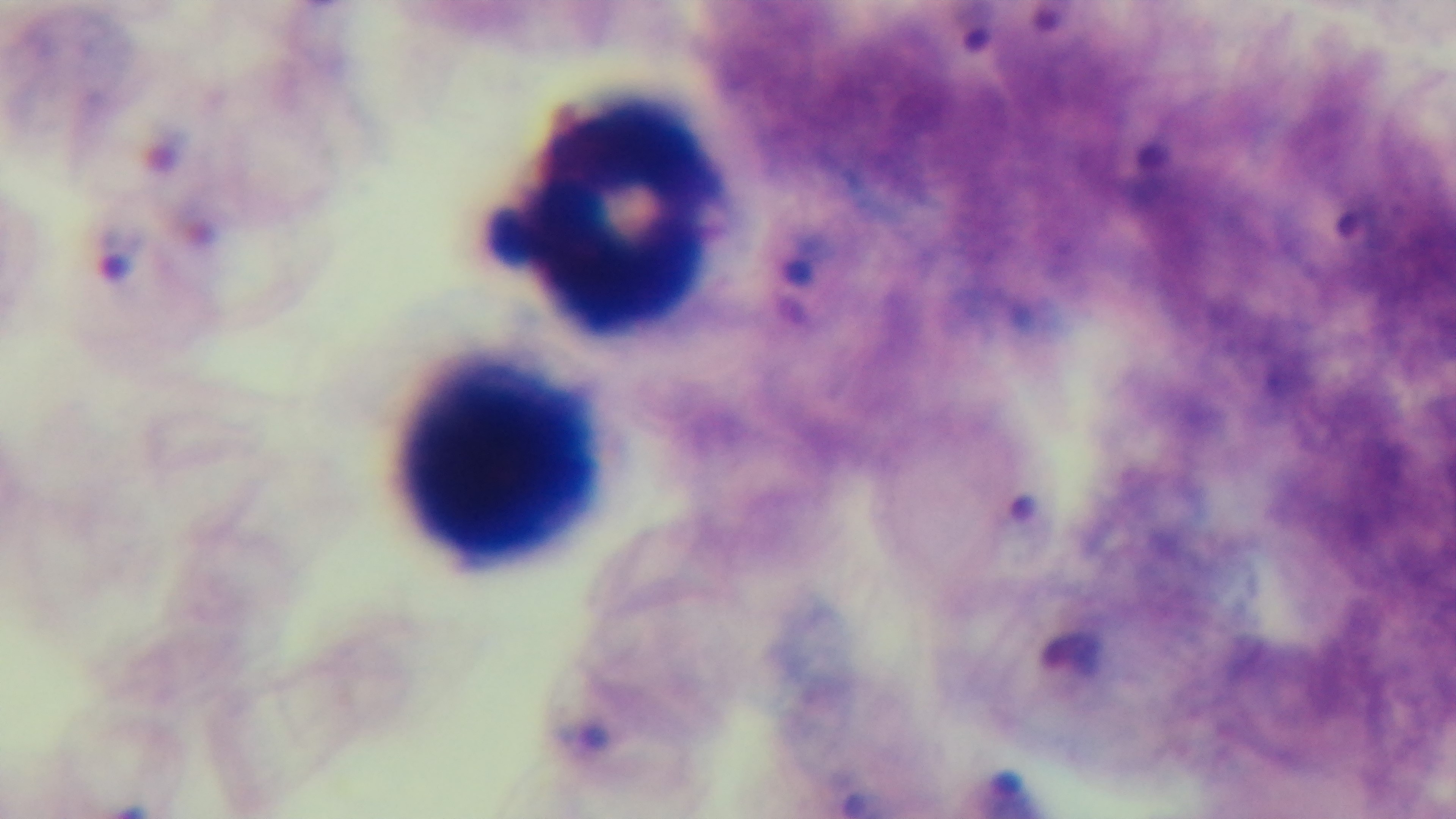
modality = light microscopy
stain = Giemsa
malaria status = infected
preparation = thick
capture = mounted 4K digital camera
field of view = one from the slide
objective = 100x oil immersion